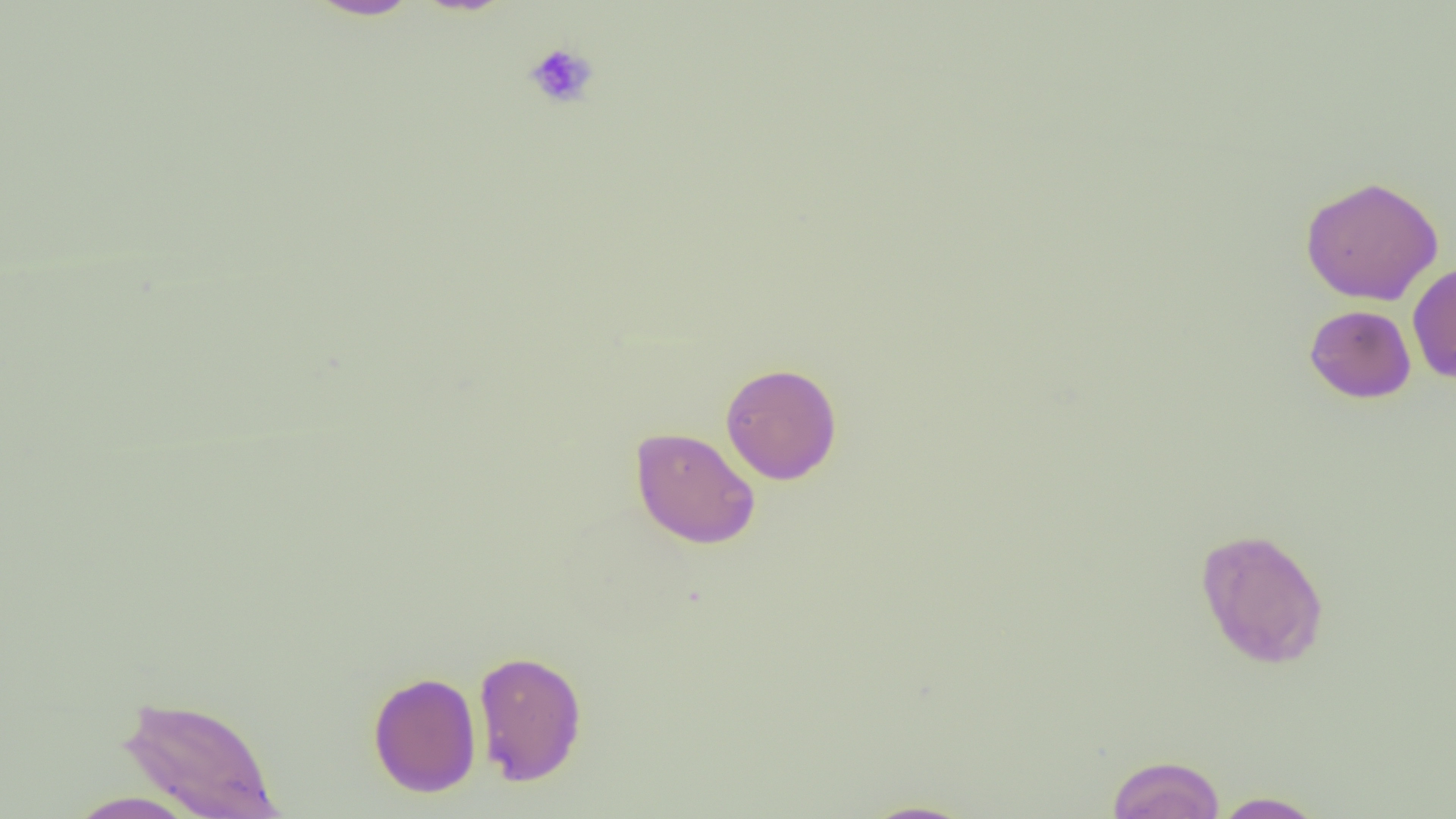

Approximate bounding boxes as (x1, y1, x2, y2) in pixels. Uninfected red blood cell locations: (305, 0, 423, 20), (1300, 175, 1444, 306), (1407, 260, 1456, 384), (1304, 304, 1416, 403), (720, 362, 842, 485), (630, 426, 761, 549), (1195, 527, 1329, 669), (473, 649, 588, 786), (368, 671, 482, 797), (118, 694, 282, 818), (1107, 754, 1226, 818), (64, 790, 202, 818), (1210, 791, 1328, 818), (857, 800, 978, 819). Platelet locations: (523, 41, 599, 110). Slide-level diagnosis: no evidence of blood parasites. Single field of view. Image is 1456×819 pixels. 1000x magnification. Thin blood smear. Light microscopy.